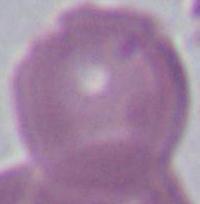
Summary:
  - Magnification: 1000x
  - Identification: erythrocyte
  - Modality: micrograph